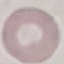
result = no malaria parasites seen
preparation = thin blood smear
capture = smartphone camera at the microscope eyepiece
image type = cell patch, automatically extracted from a larger field of view and resized to 64 × 64 pixels
stain = Giemsa